Name the parasite shown.
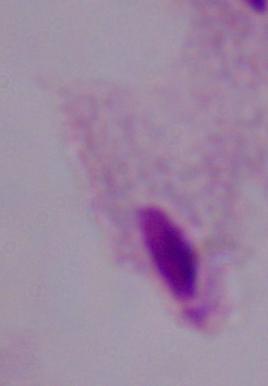

This is a trichomonad.

modality: photomicrograph
magnification: 1000x